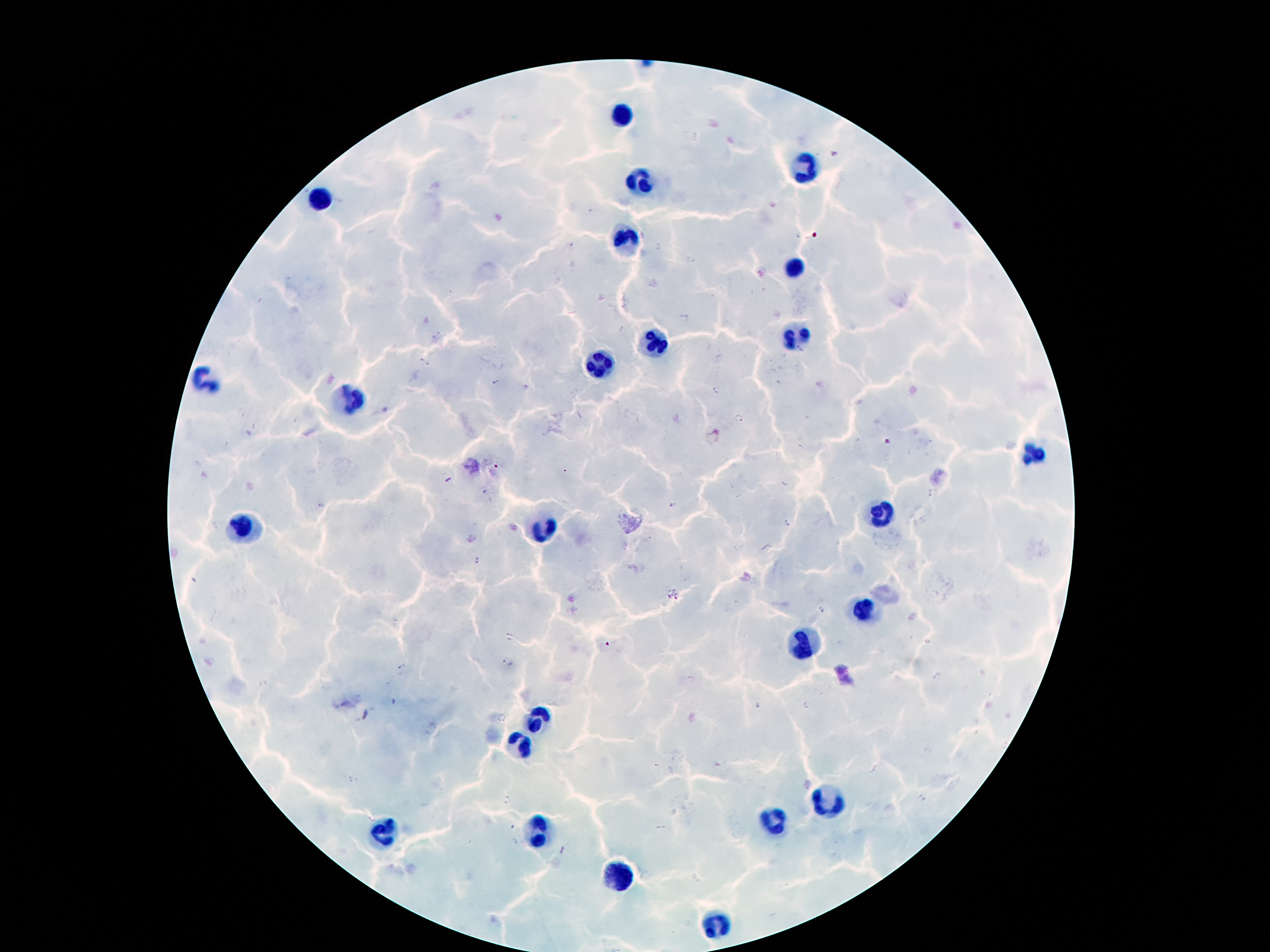
Approximate centers as [x, y] in pixels.
Summary:
  - Leukocyte locations: [616, 114], [807, 170], [641, 185], [322, 196], [627, 242], [791, 265], [796, 335], [656, 344], [601, 366], [207, 382], [351, 402], [1030, 455], [875, 514], [247, 525], [541, 530], [864, 607], [800, 647], [537, 716], [519, 742], [829, 804], [776, 819], [384, 831], [539, 833], [621, 875], [716, 926]
  - Malaria parasite locations: [570, 246], [658, 248], [691, 258], [684, 318], [496, 382], [717, 391], [741, 417], [886, 440], [498, 466], [482, 492], [931, 493], [672, 505], [786, 524], [478, 561], [669, 591], [677, 595], [822, 609], [510, 637], [926, 642], [608, 645], [507, 663], [402, 668], [936, 677], [807, 704], [757, 705], [502, 720], [506, 801], [562, 850]
  - Patient malaria status: positive for Plasmodium falciparum
  - Preparation: thick blood smear
  - Capture: smartphone through the microscope eyepiece
  - Magnification: 100x
  - Field of view: one from this slide
  - Image size: 1270×952 pixels
  - Stain: Giemsa